Classify this cell by malaria status.
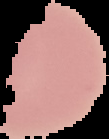
It is uninfected.

Summary:
  - Preparation: thin blood smear
  - Image size: 109×139 pixels
  - Image type: cell region segmented out of the field of view; surrounding area masked to black